Classify this cell by malaria status.
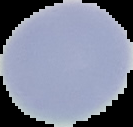

Uninfected.

From a thin blood film. Image is 133×127 pixels. Cell region segmented out of the field of view; the surrounding area is masked to black.